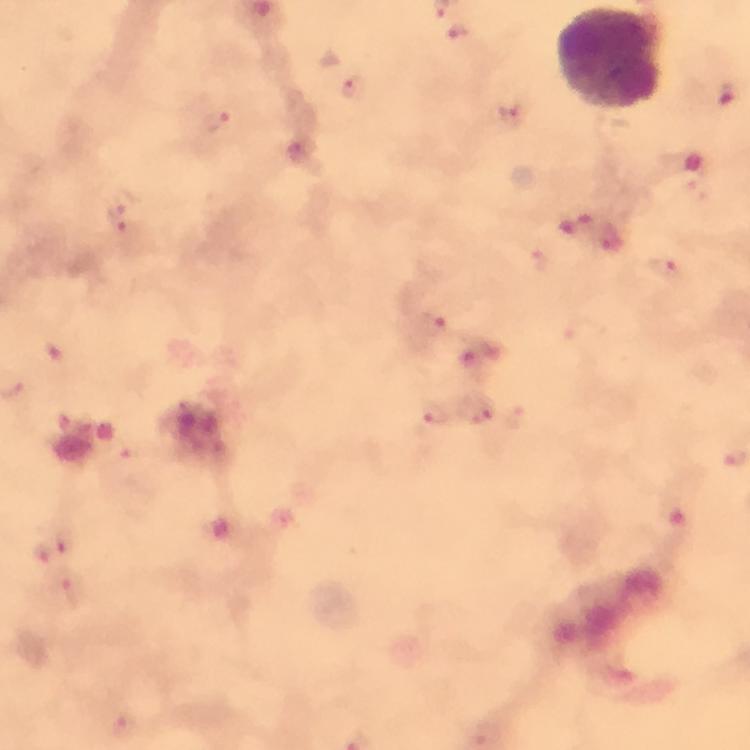

immersion oil = applied
preparation = thick blood smear
cropped from = a single field of view
context = from a diagnostic examination for malaria
stain = Giemsa
malaria parasite locations = approximate centers as {x, y} in pixels: {457, 33}, {355, 86}, {728, 98}, {511, 115}, {215, 120}, {120, 213}, {662, 269}, {434, 324}, {434, 413}, {476, 413}, {732, 451}, {42, 551}, {71, 593}, {124, 726}, {485, 734}
image size = 750×750 pixels
capture = smartphone camera through the microscope
magnification = 100x
leukocyte locations = approximate centers as {x, y} in pixels: {609, 58}